Give the position of every Plasmodium parasite visible.
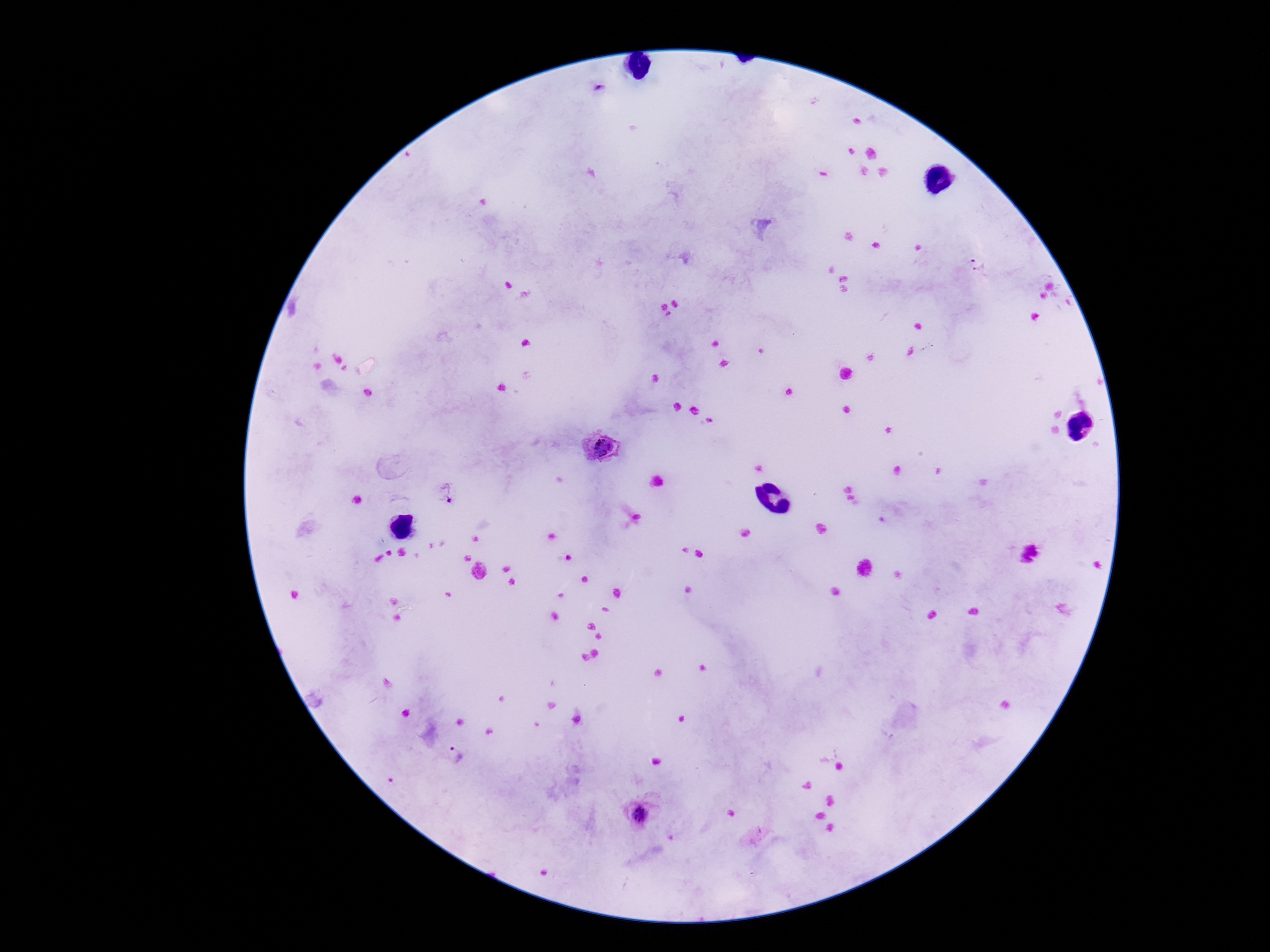
Approximate centers as [x, y] in pixels.
Plasmodium parasites: [978, 265], [600, 451], [444, 496], [459, 757], [638, 815].

Single field of view. Image is 1270×952 pixels. 100x magnification. Thick blood film. Patient malaria status: infected. Smartphone photograph taken through the microscope eyepiece. Giemsa stain.